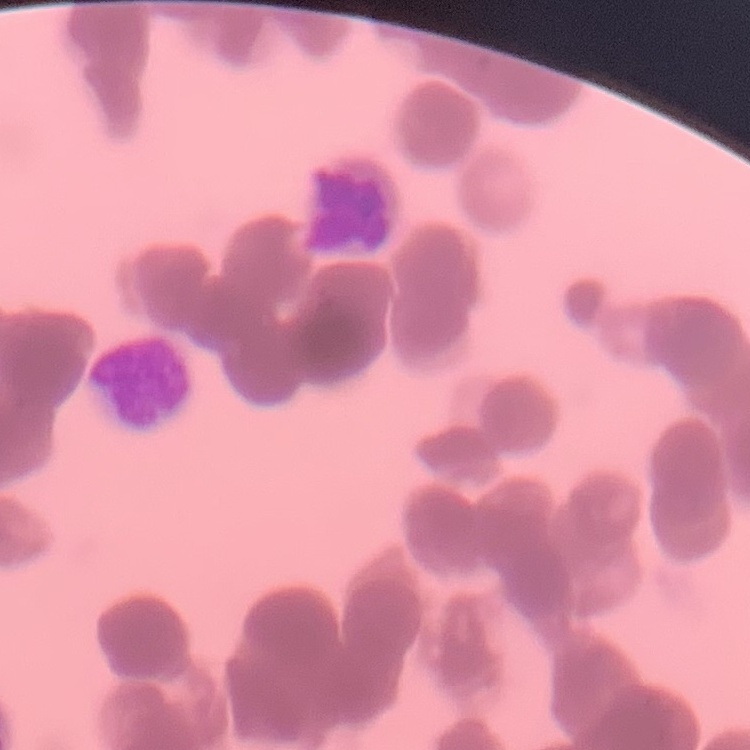

Summary:
  - Red blood cell morphology: rouleaux formation
  - Preparation: thin peripheral smear
  - Stain: Field's or Giemsa
  - Image type: square crop of a larger photomicrograph